Report the malaria status of this cell.
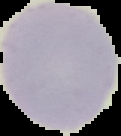
Uninfected.

Summary:
  - Image size: 121×136 pixels
  - Preparation: thin blood smear
  - Image type: segmented cell region on a black background